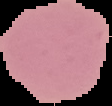

Image is 112×106 pixels. Segmented cell region on a black background. From a thin blood film. Result: no Plasmodium parasites detected.